Assess this cell for malaria.
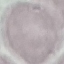
Uninfected.

Thin smear of blood. Giemsa stain. Automatically extracted cell patch, resized to 64 × 64 pixels. Photographed with a smartphone camera at the microscope eyepiece.